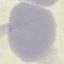 Malaria status: uninfected. Thin blood film. Giemsa stain. Acquired by smartphone through the microscope eyepiece. Cell patch, automatically extracted from a larger field of view and resized to 64 × 64 pixels.